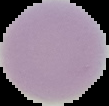

From a thin blood smear. Image is 109×106 pixels. Malaria status: uninfected. Cell region segmented out of the field of view; the surrounding area is masked to black.